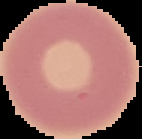

image_type: cell region segmented out of the field of view; surrounding area masked to black
image_size: 142×139 pixels
preparation: thin blood smear
result: negative for malaria parasites